State which cell type is depicted.
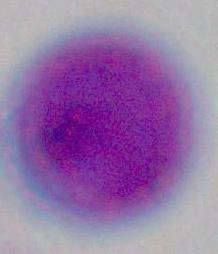

This is a leukocyte.

Summary:
  - Magnification: 1000x
  - Modality: micrograph